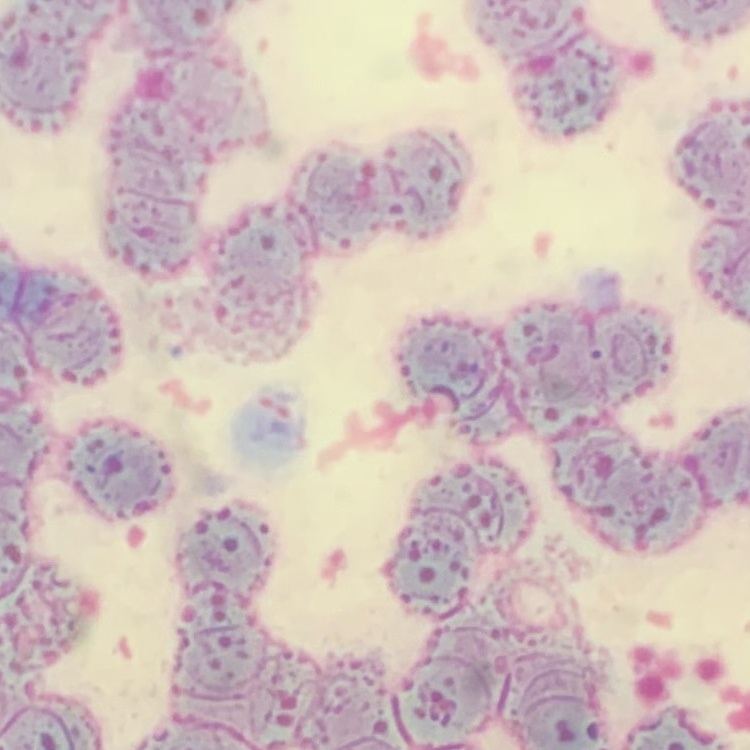 The erythrocytes exhibit rouleaux formation. Square crop of a larger photomicrograph. Thin blood film. Field's or Giemsa stain.